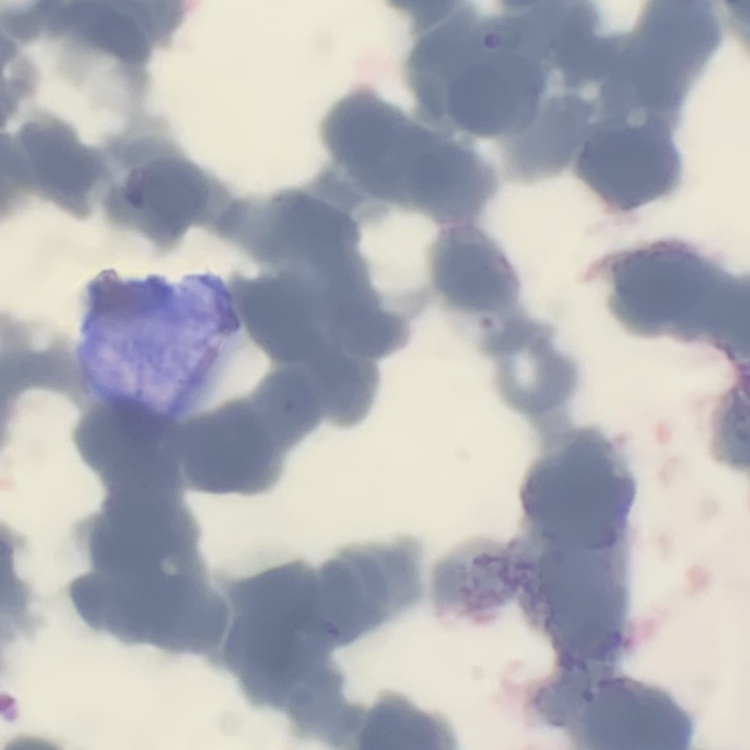
erythrocyte_morphology: rouleaux formation
preparation: thin blood film
image_type: square crop of a larger photomicrograph
stain: Field's or Giemsa